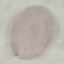

Summary:
  - Malaria status: uninfected
  - Capture: smartphone camera at the microscope eyepiece
  - Image type: automatically extracted cell patch, resized to 64 × 64 pixels
  - Preparation: thin blood film
  - Stain: Giemsa